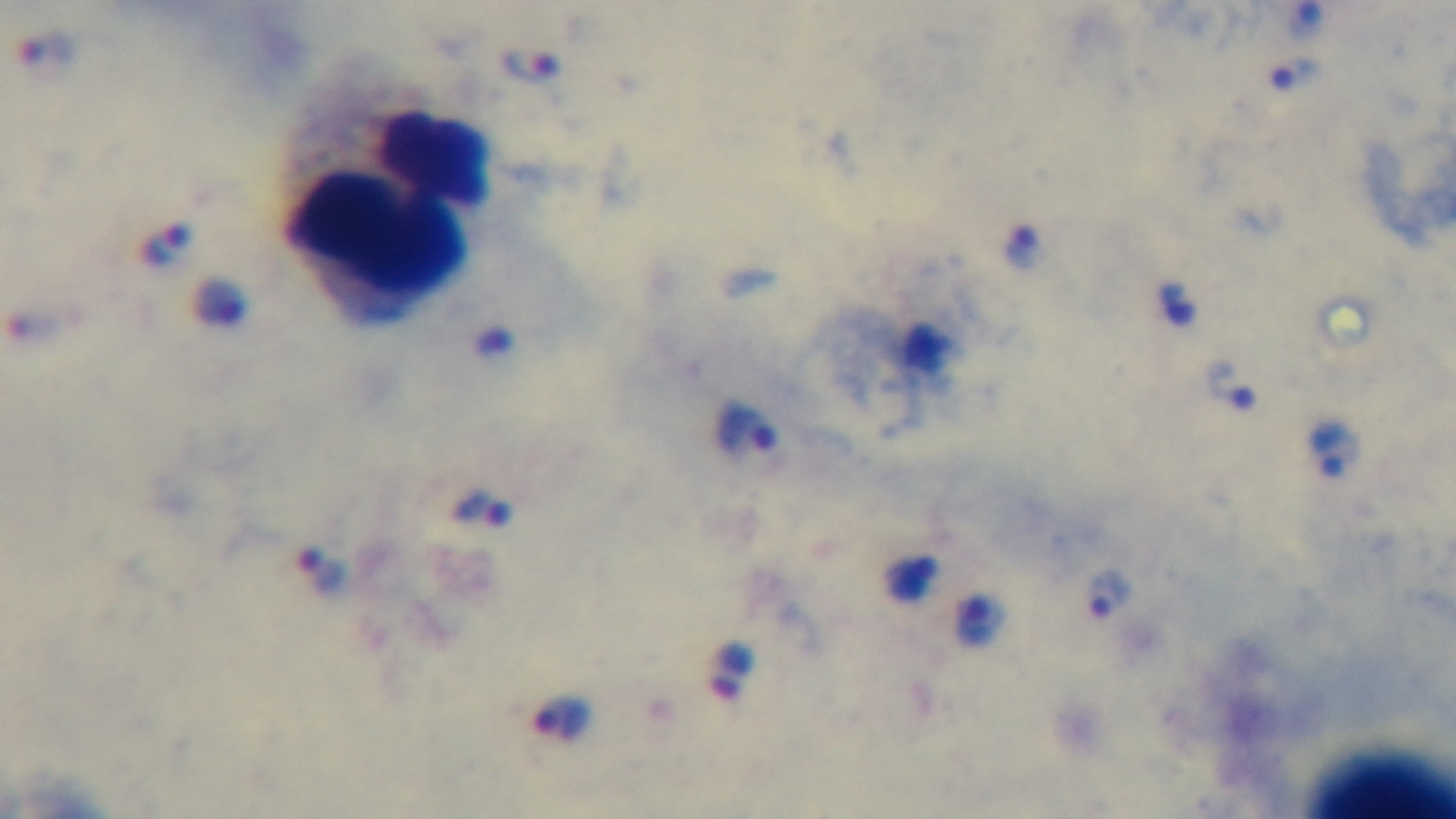
Oil-immersion objective, 100x. Light microscopy. Giemsa stain. Single field of view. Mounted 4K digital camera. Malaria status: infected. Preparation: thick blood film.